Assess the morphology of the red blood cells.
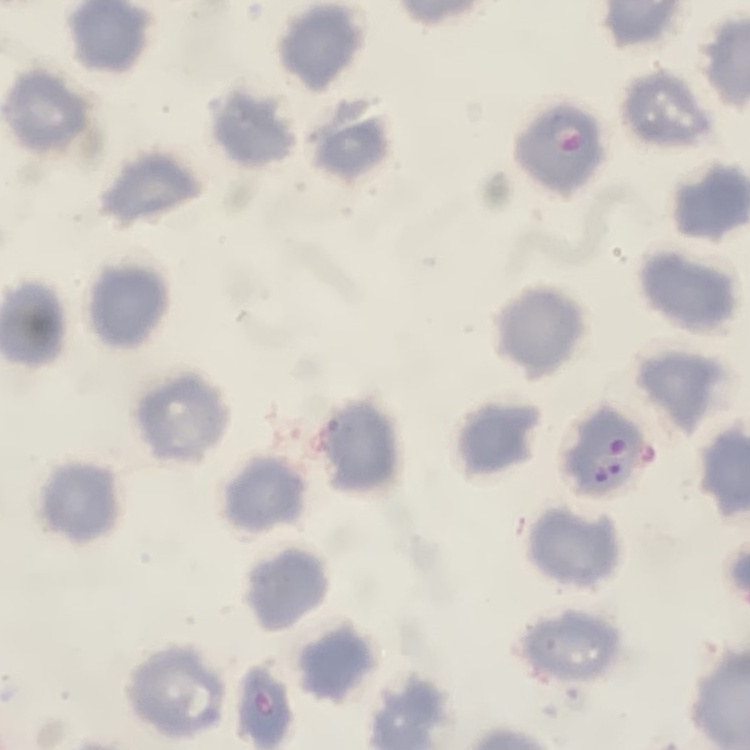
They show no rouleaux formation.

{
  "image_type": "square crop of a larger photomicrograph",
  "preparation": "thin peripheral smear",
  "stain": "Field's or Giemsa"
}